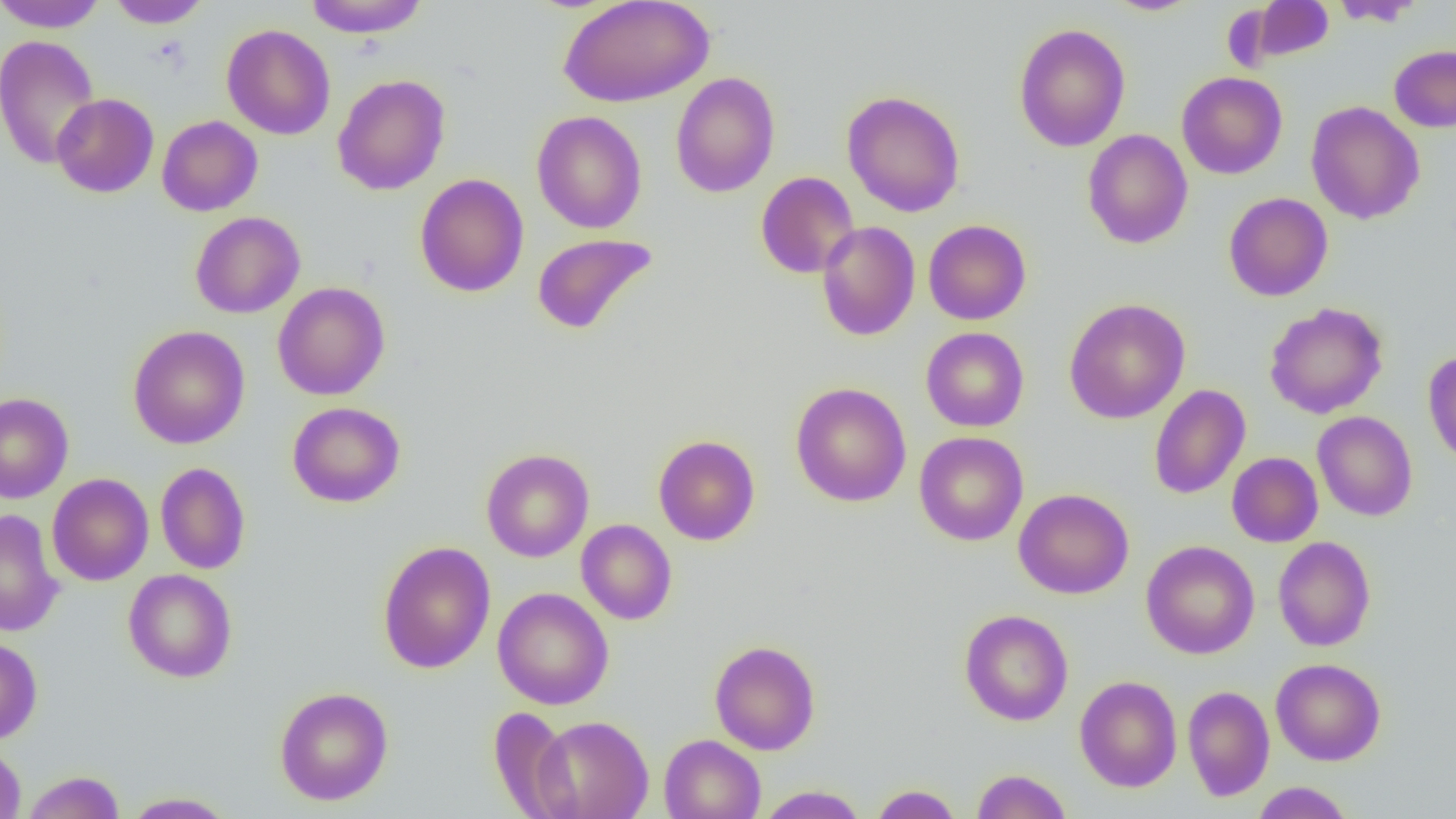
slide-level diagnosis = negative for blood parasites
uninfected red blood cell locations = approximate bounding boxes as (x1, y1, x2, y2) in pixels: (0, 0, 108, 32), (303, 0, 430, 38), (557, 0, 715, 108), (1102, 0, 1205, 16), (1250, 0, 1336, 62), (1329, 0, 1426, 27), (108, 1, 212, 29), (1013, 23, 1130, 152), (221, 24, 335, 140), (0, 34, 101, 170), (1389, 45, 1456, 132), (670, 72, 780, 198), (1176, 72, 1287, 179), (332, 74, 450, 196), (842, 90, 965, 217), (51, 93, 159, 198), (1305, 101, 1425, 224), (532, 110, 647, 234), (157, 115, 263, 216), (1082, 129, 1193, 249), (755, 172, 859, 278), (414, 173, 529, 297), (1223, 192, 1333, 301), (190, 211, 305, 318), (923, 219, 1031, 325), (817, 221, 920, 341), (531, 233, 657, 335), (272, 282, 390, 400), (1065, 298, 1190, 424), (1264, 302, 1388, 419), (128, 325, 250, 449), (920, 327, 1030, 432), (1423, 350, 1456, 468), (790, 382, 912, 507), (1149, 384, 1251, 500), (0, 393, 74, 503), (287, 401, 405, 508), (1312, 411, 1418, 521), (914, 431, 1029, 546), (652, 434, 761, 546), (480, 448, 594, 562), (1227, 452, 1323, 547), (155, 462, 251, 575), (47, 473, 154, 586), (1013, 488, 1134, 599), (1, 509, 65, 637), (576, 519, 677, 625), (1273, 536, 1376, 652), (1141, 540, 1260, 659), (376, 541, 496, 674), (123, 569, 237, 683), (493, 587, 614, 710), (959, 609, 1073, 726), (0, 637, 42, 744), (709, 640, 821, 755), (1271, 657, 1386, 766), (1074, 675, 1182, 792), (1182, 685, 1275, 802), (274, 686, 394, 806), (488, 706, 577, 817), (533, 715, 654, 818), (659, 734, 766, 819), (0, 743, 26, 818), (971, 769, 1072, 819), (20, 770, 126, 818), (1250, 782, 1355, 819), (869, 784, 963, 818), (755, 785, 868, 819), (121, 791, 237, 818)
image size = 1456×819 pixels
field of view = one of a larger specimen
preparation = thin blood smear
magnification = 1000x
modality = light microscopy